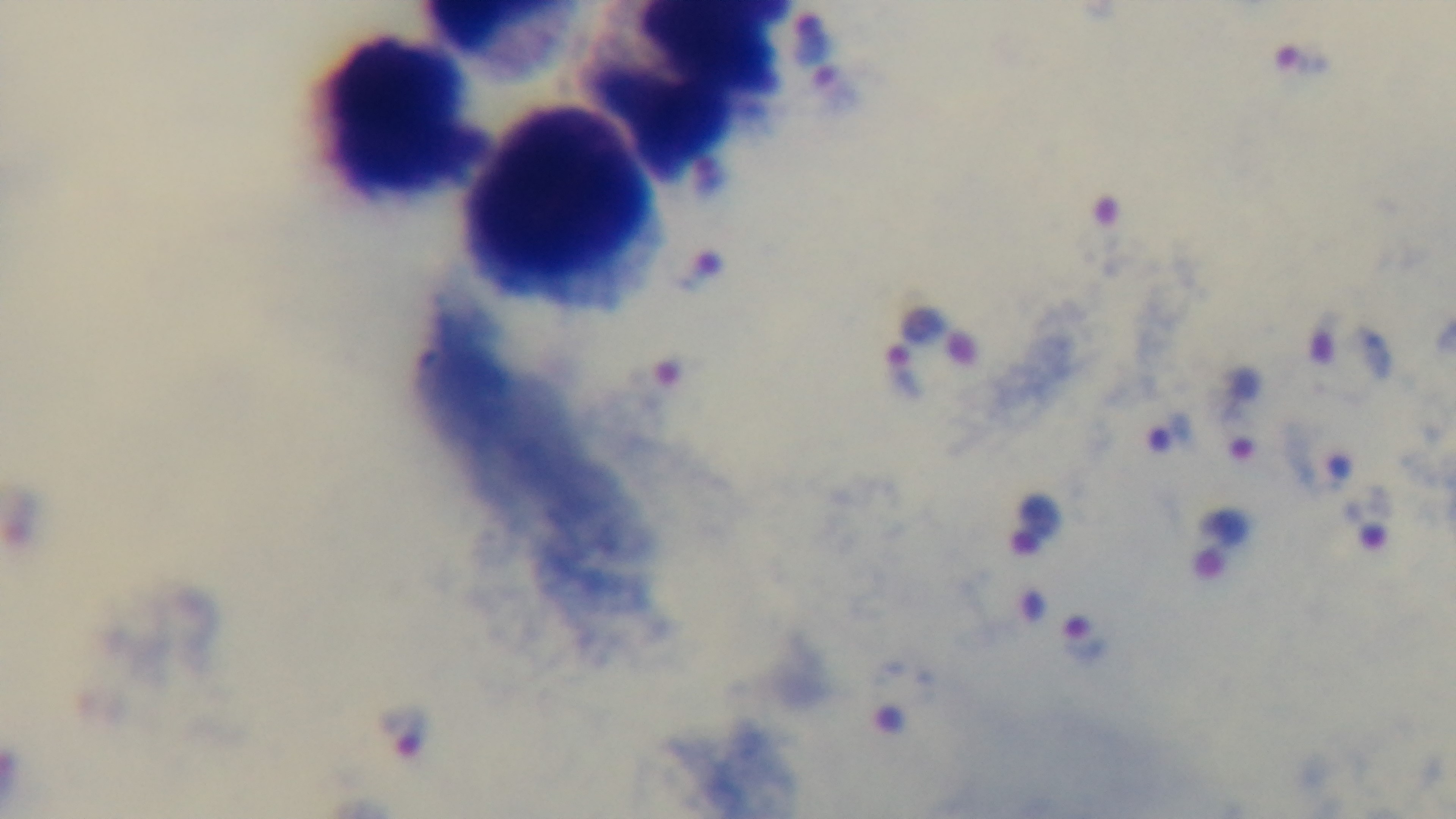 Giemsa-stained. Single field of view. Mounted 4K digital camera. Preparation: thick blood film. Oil-immersion objective, 100x. Malaria status: positive. Photomicrograph.